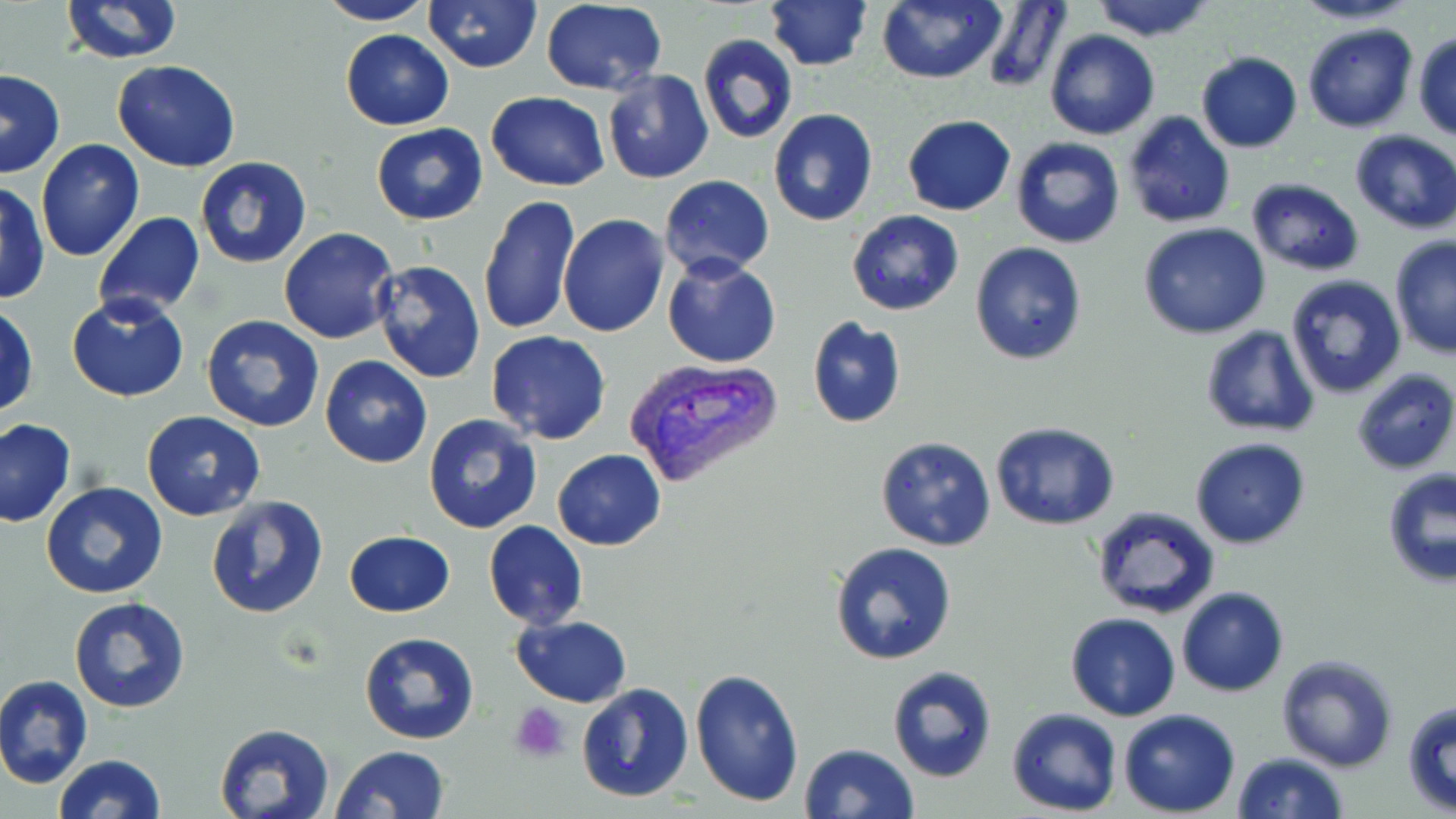
Summary:
  - Coordinate format: approximate bounding boxes as (x1,y1)-(x2,y2) corner pairs in pixels
  - Platelet locations: (511,703)-(572,763)
  - Uninfected red blood cell locations: (59,0)-(183,64), (424,0)-(542,73), (765,0)-(873,72), (876,0)-(1004,84), (1088,0)-(1218,42), (1287,0)-(1426,27), (315,1)-(433,26), (979,1)-(1072,93), (538,2)-(669,94), (1301,23)-(1417,132), (340,29)-(455,129), (1044,30)-(1160,141), (1412,32)-(1456,142), (697,35)-(798,144), (1195,51)-(1302,152), (112,60)-(240,171), (1,69)-(65,178), (603,71)-(714,184), (486,92)-(609,192), (769,108)-(878,227), (1122,111)-(1236,229), (902,114)-(1015,215), (372,124)-(488,224), (1349,130)-(1456,234), (1009,137)-(1126,250), (35,140)-(146,261), (195,157)-(312,268), (659,176)-(775,279), (1245,178)-(1364,275), (1,181)-(50,304), (476,196)-(580,334), (846,210)-(963,316), (93,212)-(205,318), (558,213)-(668,337), (1138,221)-(1271,340), (278,228)-(399,345), (1389,235)-(1456,358), (969,243)-(1087,366), (662,253)-(781,369), (371,260)-(486,384), (1286,275)-(1407,399), (66,293)-(192,402), (1,303)-(39,418), (202,314)-(326,434), (806,316)-(907,428), (1201,327)-(1322,438), (486,331)-(612,445), (319,357)-(434,470), (1352,368)-(1456,474), (141,409)-(265,521), (423,413)-(542,533), (0,417)-(75,528), (990,421)-(1121,531), (875,436)-(998,553), (1190,437)-(1310,549), (553,449)-(665,551), (1381,469)-(1455,589), (40,482)-(168,600), (203,494)-(330,619), (1089,507)-(1221,622), (482,521)-(588,630), (344,529)-(454,618), (830,540)-(959,666), (1177,587)-(1289,697), (70,597)-(192,713), (1065,613)-(1181,721), (513,615)-(631,706), (359,632)-(481,746), (1275,653)-(1397,771), (886,665)-(997,783), (689,667)-(804,808), (0,675)-(93,787), (575,681)-(693,803), (1402,700)-(1456,815), (1007,708)-(1123,815), (1118,708)-(1240,817), (214,723)-(335,819), (800,743)-(919,819), (331,745)-(451,819), (1231,751)-(1348,819), (53,754)-(166,819)
  - Plasmodium vivax-infected red blood cell locations: (619,357)-(785,489)
  - Slide-level diagnosis: Plasmodium vivax
  - Image size: 1456×819 pixels
  - Field of view: one of a larger specimen
  - Magnification: 1000x
  - Stain: May-Grünwald-Giemsa
  - Modality: light microscopy
  - Preparation: thin blood film